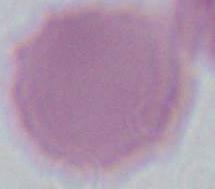

Summary:
  - Modality: photomicrograph
  - Magnification: 1000x
  - Identification: erythrocyte